State which cell type is depicted.
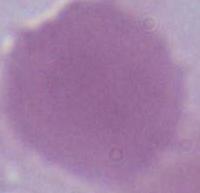
This is an erythrocyte.

Photomicrograph. 1000x magnification.